Report the malaria status of this cell.
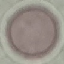
It is uninfected.

Thin blood film. Acquired by smartphone through the microscope eyepiece. Automatically extracted cell patch, resized to 64 × 64 pixels. Giemsa-stained preparation.